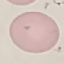
Summary:
  - Result: no malaria parasites seen
  - Preparation: thin blood smear
  - Stain: Giemsa
  - Image type: automatically extracted cell patch, resized to 64 × 64 pixels
  - Capture: smartphone through the microscope eyepiece